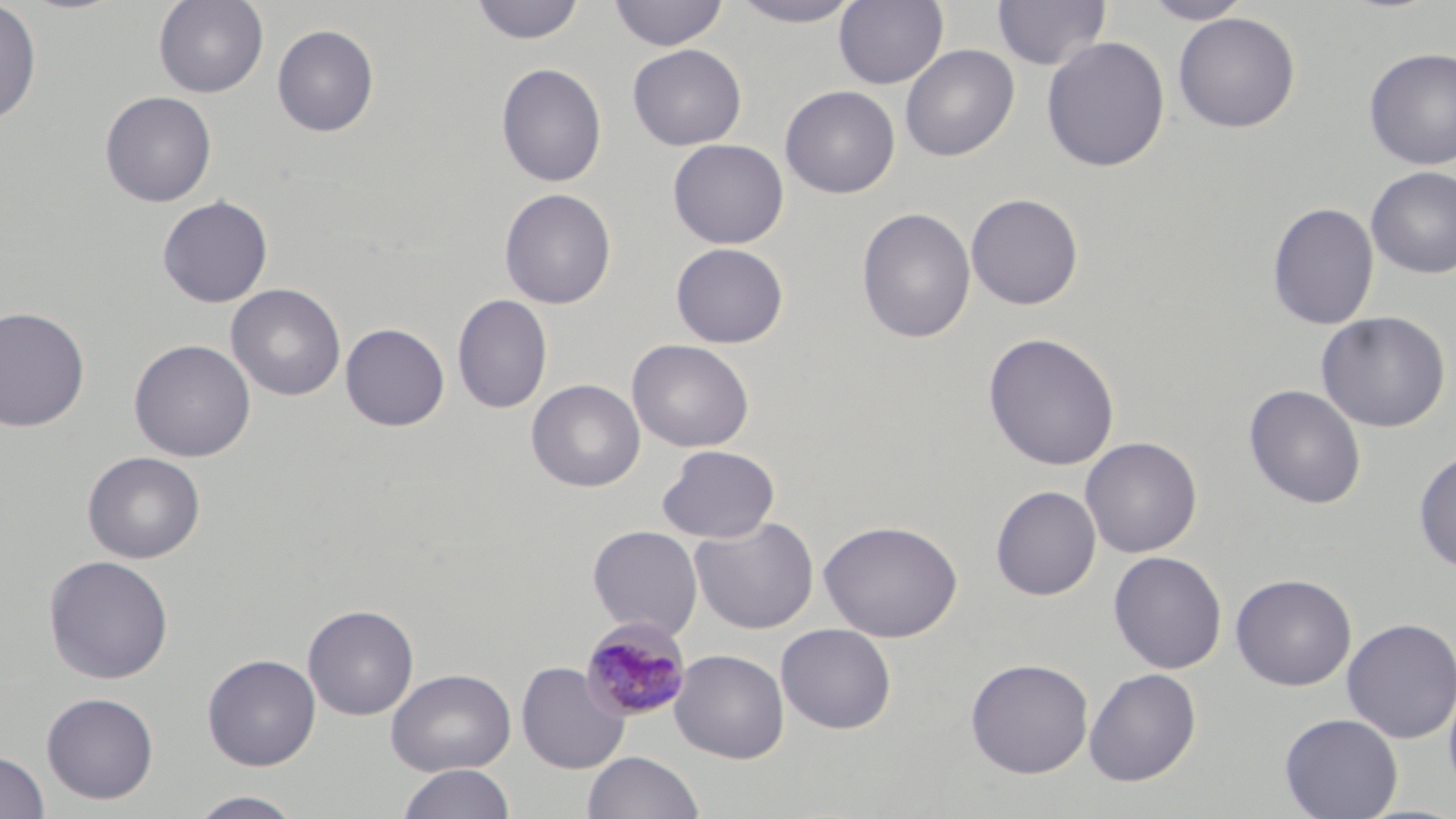
Approximate bounding boxes as [x1, y1, x2, y2] in pixels. Uninfected red blood cell locations: [153, 0, 269, 98], [470, 0, 584, 45], [608, 0, 729, 51], [728, 0, 866, 27], [834, 0, 949, 89], [991, 0, 1111, 71], [1141, 0, 1254, 24], [0, 1, 42, 126], [1173, 12, 1300, 133], [272, 24, 379, 137], [1041, 36, 1171, 172], [627, 44, 746, 150], [900, 44, 1019, 161], [1363, 47, 1456, 170], [496, 63, 607, 187], [779, 85, 900, 199], [100, 91, 217, 207], [667, 138, 789, 249], [1366, 166, 1456, 279], [499, 187, 616, 308], [965, 192, 1083, 310], [157, 195, 273, 308], [1266, 202, 1380, 330], [856, 207, 976, 344], [671, 242, 789, 348], [226, 283, 346, 401], [451, 294, 552, 414], [0, 306, 91, 432], [1316, 311, 1451, 433], [340, 322, 450, 431], [983, 331, 1120, 471], [627, 338, 754, 452], [129, 339, 255, 462], [526, 379, 646, 492], [1243, 384, 1366, 509], [1080, 436, 1202, 558], [657, 445, 780, 543], [1413, 448, 1456, 573], [82, 450, 205, 563], [991, 485, 1101, 600], [690, 516, 819, 634], [819, 519, 963, 643], [587, 525, 703, 639], [1108, 550, 1227, 674], [43, 554, 174, 684], [1230, 573, 1356, 691], [303, 604, 418, 720], [1341, 617, 1455, 743], [776, 623, 897, 734], [669, 649, 790, 763], [202, 654, 321, 770], [965, 658, 1094, 779], [516, 661, 629, 774], [1084, 667, 1201, 786], [386, 668, 516, 776], [1442, 679, 1456, 797], [41, 692, 160, 804], [1279, 712, 1403, 819], [0, 750, 50, 819], [582, 750, 704, 819], [396, 763, 517, 819], [187, 790, 306, 819]. Plasmodium malariae-infected red blood cell locations: [580, 618, 692, 721]. Slide-level diagnosis: Plasmodium malariae. Thin blood film. One field of a larger specimen. 1000x magnification. May-Grünwald-Giemsa-stained preparation. Optical microscopy. Image is 1456×819 pixels.